Outline each blood parasite and name the species.
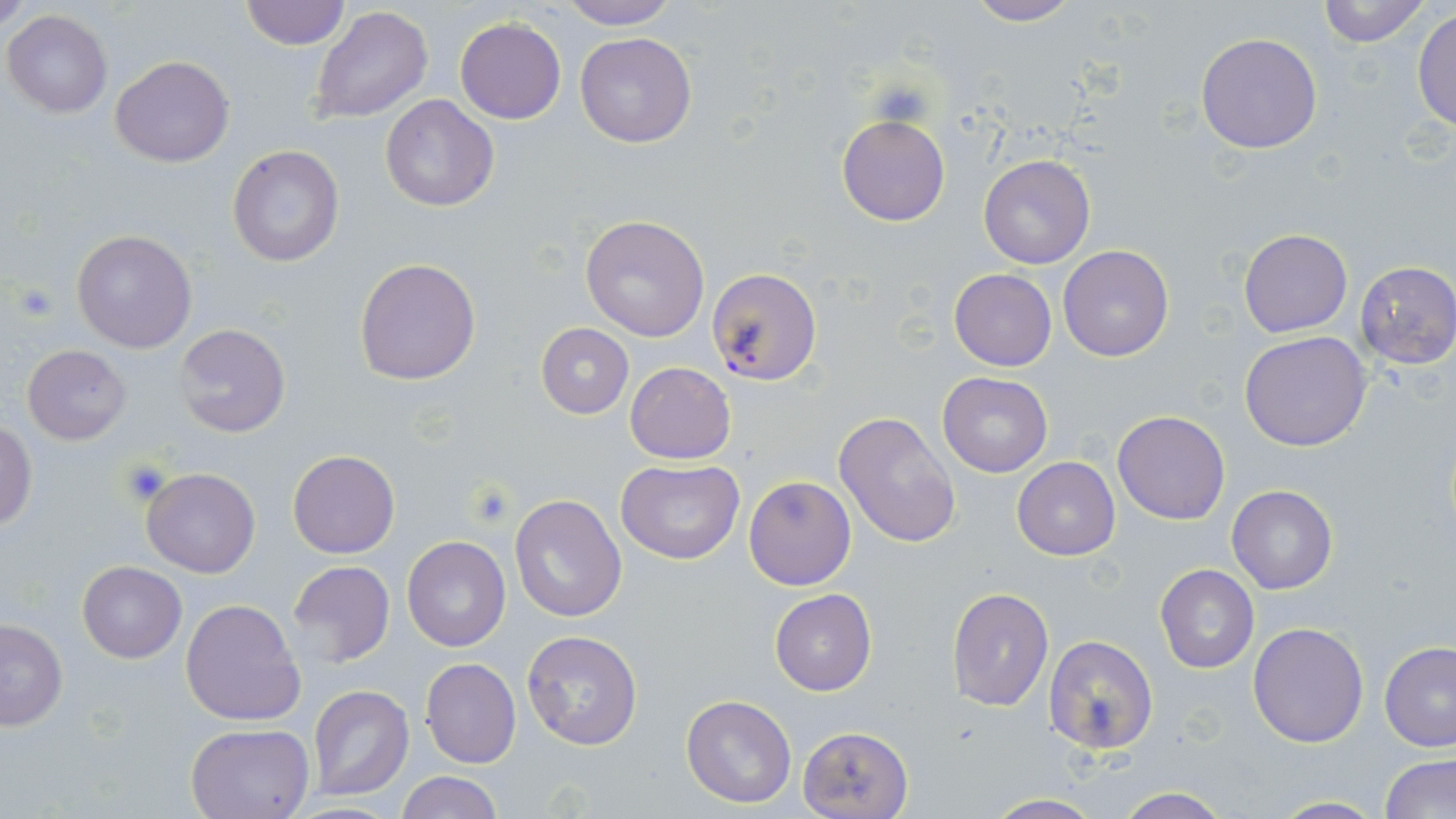
Approximate bounding boxes as (x1, y1, x2, y2) in pixels.
Plasmodium falciparum-infected red blood cells: (705, 267, 822, 388).
No Plasmodium ovale, Plasmodium malariae, Plasmodium vivax, Babesia divergens, or Trypanosoma brucei observed.

slide-level diagnosis = Plasmodium falciparum
field of view = single
image size = 1456×819 pixels
modality = optical microscopy
magnification = 1000x
uninfected red blood cell locations = approximate bounding boxes as (x1, y1, x2, y2) in pixels: (1, 0, 31, 28), (558, 0, 680, 29), (1315, 0, 1433, 47), (239, 1, 348, 49), (962, 1, 1082, 26), (309, 4, 434, 124), (1413, 7, 1456, 135), (3, 10, 112, 117), (455, 17, 566, 123), (575, 31, 698, 148), (1196, 31, 1323, 154), (110, 55, 234, 168), (380, 94, 499, 212), (837, 112, 950, 226), (227, 145, 344, 266), (979, 154, 1095, 269), (580, 214, 710, 340), (1238, 228, 1352, 338), (70, 229, 198, 353), (1058, 245, 1173, 364), (354, 257, 482, 387), (1354, 261, 1456, 369), (949, 268, 1056, 371), (175, 323, 290, 438), (536, 323, 634, 418), (1239, 331, 1372, 451), (22, 344, 132, 444), (629, 362, 739, 464), (937, 371, 1052, 476), (1112, 410, 1230, 525), (834, 411, 962, 549), (0, 418, 39, 530), (288, 450, 400, 559), (1012, 457, 1120, 560), (616, 459, 744, 566), (141, 466, 259, 578), (743, 475, 856, 590), (1227, 485, 1337, 594), (510, 494, 626, 621), (402, 536, 510, 651), (77, 560, 186, 662), (288, 560, 395, 667), (1155, 564, 1259, 673), (946, 587, 1054, 712), (770, 589, 876, 695), (180, 599, 306, 726), (0, 619, 69, 732), (1247, 621, 1370, 748), (520, 631, 643, 751), (1043, 635, 1157, 754), (1379, 640, 1456, 751), (420, 658, 521, 768), (307, 685, 415, 801), (680, 695, 796, 807), (184, 722, 315, 819), (797, 726, 913, 818), (1379, 751, 1456, 817), (395, 771, 503, 819), (1112, 789, 1234, 819), (979, 794, 1108, 818), (1265, 795, 1388, 818)
platelet locations = approximate bounding boxes as (x1, y1, x2, y2) in pixels: (13, 281, 58, 322), (115, 459, 174, 504)
preparation = thin blood film
stain = May-Grünwald-Giemsa